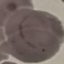

Summary:
  - Result: malaria parasites identified
  - Image type: automatically extracted cell patch, resized to 64 × 64 pixels
  - Stain: Giemsa
  - Preparation: thin blood smear
  - Capture: smartphone camera at the microscope eyepiece